Report the malaria status of this cell.
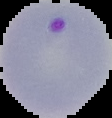
Parasitized.

Image is 112×118 pixels. From a thin blood film. Segmented cell region on a black background.